Name the parasite shown.
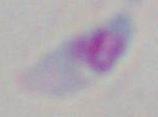
This is Toxoplasma gondii.

modality: micrograph
magnification: 1000x